Classify this cell by malaria status.
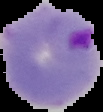
Parasitized.

Summary:
  - Image type: segmented cell region with the area outside set to black
  - Image size: 103×112 pixels
  - Preparation: thin blood smear